Assess this cell for malaria.
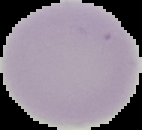
Uninfected.

Segmented cell region on a black background. From a thin blood smear. Image is 142×130 pixels.